Assess this cell for malaria.
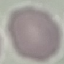

It is uninfected.

image type = cell patch, automatically extracted from a larger field of view and resized to 64 × 64 pixels
capture = smartphone camera at the microscope eyepiece
stain = Giemsa
preparation = thin blood film